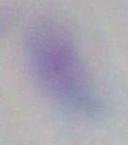
modality = micrograph
magnification = 1000x
identification = Toxoplasma gondii